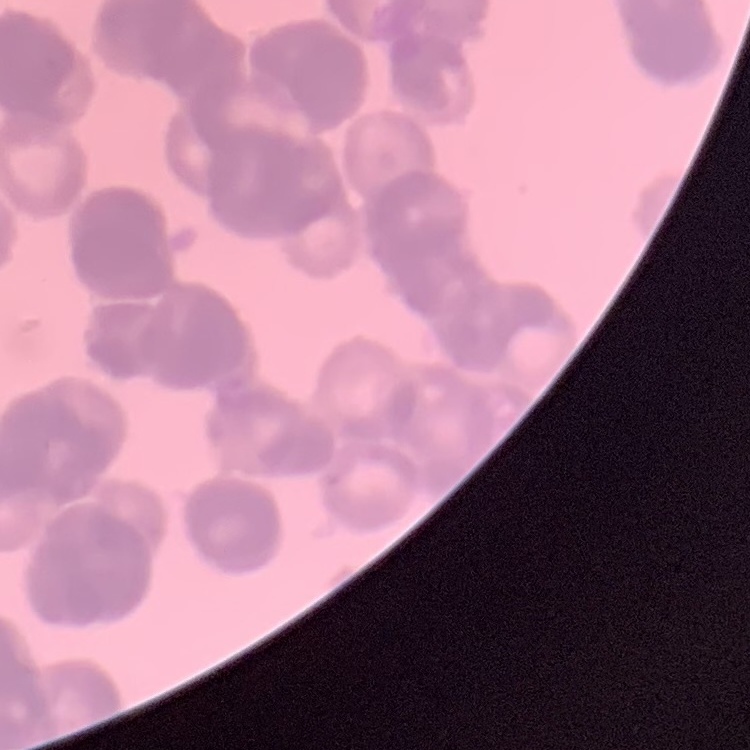

erythrocyte morphology = rouleaux formation
image type = one tile cut from a larger photomicrograph
preparation = thin peripheral smear
stain = Field's or Giemsa